Classify this cell by malaria status.
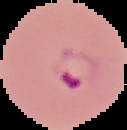
It is parasitized.

{
  "image_size": "127×130 pixels",
  "preparation": "thin blood smear",
  "image_type": "segmented cell region on a black background"
}